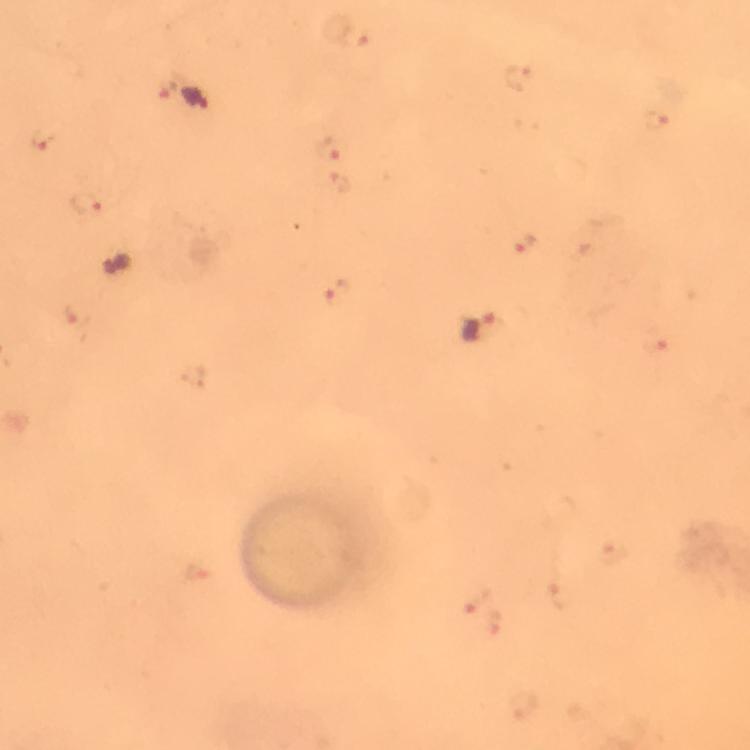
Approximate centers as (x, y) in pixels.
Summary:
  - Plasmodium parasite locations: (355, 39), (195, 100), (657, 121), (41, 138), (333, 147), (83, 203), (524, 244), (336, 294), (484, 329), (654, 343), (476, 601)
  - Magnification: 100x
  - Capture: smartphone mounted on the microscope
  - Cropped from: a single field of view
  - Preparation: thick smear
  - Context: from a diagnostic examination for malaria
  - Immersion oil: used
  - Image size: 750×750 pixels
  - Stain: Giemsa